Assess the morphology of the erythrocytes.
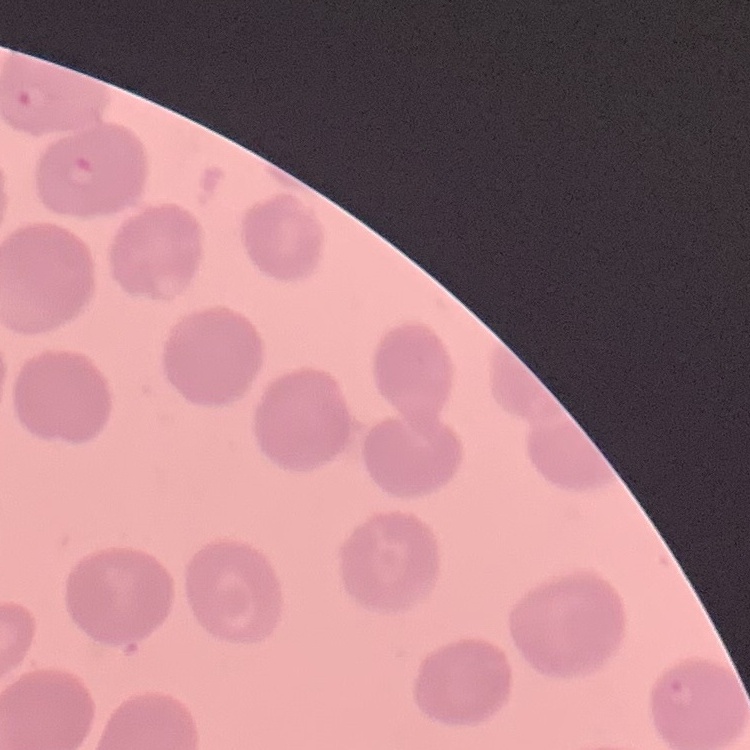

No rouleaux formation.

Summary:
  - Stain: Field's or Giemsa
  - Preparation: thin peripheral smear
  - Image type: one tile cut from a larger photomicrograph